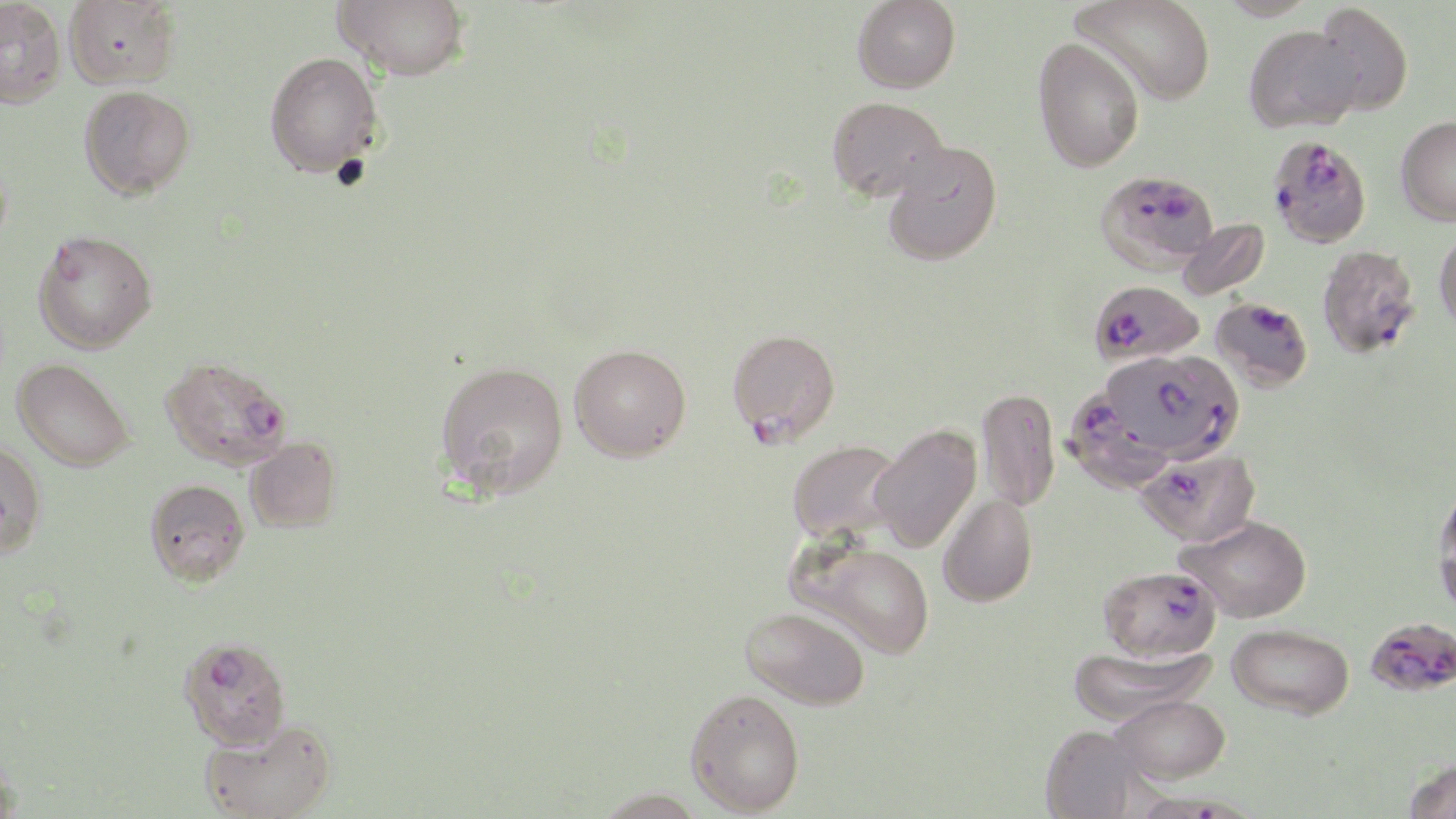 Approximate bounding boxes as [x1, y1, x2, y2] in pixels. Plasmodium falciparum-infected red blood cell locations: [1266, 134, 1372, 248], [1096, 169, 1218, 274], [1317, 244, 1422, 359], [1089, 279, 1205, 366], [1210, 296, 1314, 393], [726, 328, 841, 447], [1100, 349, 1244, 462], [160, 355, 292, 472], [1063, 386, 1177, 495], [1136, 446, 1261, 547], [1098, 564, 1222, 662], [1365, 616, 1456, 698], [178, 636, 292, 750], [1137, 788, 1253, 819]. Uninfected red blood cell locations: [0, 0, 66, 109], [64, 0, 181, 89], [334, 0, 470, 81], [852, 0, 961, 94], [1071, 0, 1216, 106], [1215, 0, 1322, 21], [1314, 3, 1414, 117], [1243, 24, 1364, 133], [1032, 37, 1144, 173], [264, 52, 384, 178], [79, 85, 195, 199], [826, 95, 949, 202], [1395, 115, 1456, 226], [881, 141, 1003, 266], [1176, 218, 1270, 302], [33, 228, 158, 353], [1434, 228, 1456, 335], [569, 344, 691, 462], [12, 358, 135, 472], [434, 360, 569, 501], [977, 386, 1060, 513], [869, 424, 981, 554], [245, 437, 342, 533], [0, 438, 48, 559], [787, 438, 903, 543], [144, 478, 250, 586], [1433, 485, 1456, 610], [937, 493, 1037, 607], [1179, 515, 1313, 622], [790, 539, 936, 659], [741, 606, 870, 710], [1227, 623, 1354, 720], [1067, 644, 1215, 725], [685, 688, 805, 815], [1111, 693, 1230, 783], [200, 716, 338, 819], [1039, 724, 1145, 818], [1404, 758, 1456, 819]. Slide-level diagnosis: Plasmodium falciparum. Image is 1456×819 pixels. Thin blood smear. Light microscopy. Captured at 1000x magnification. May-Grünwald-Giemsa stain. One field of a larger specimen.